Name the blood parasite species.
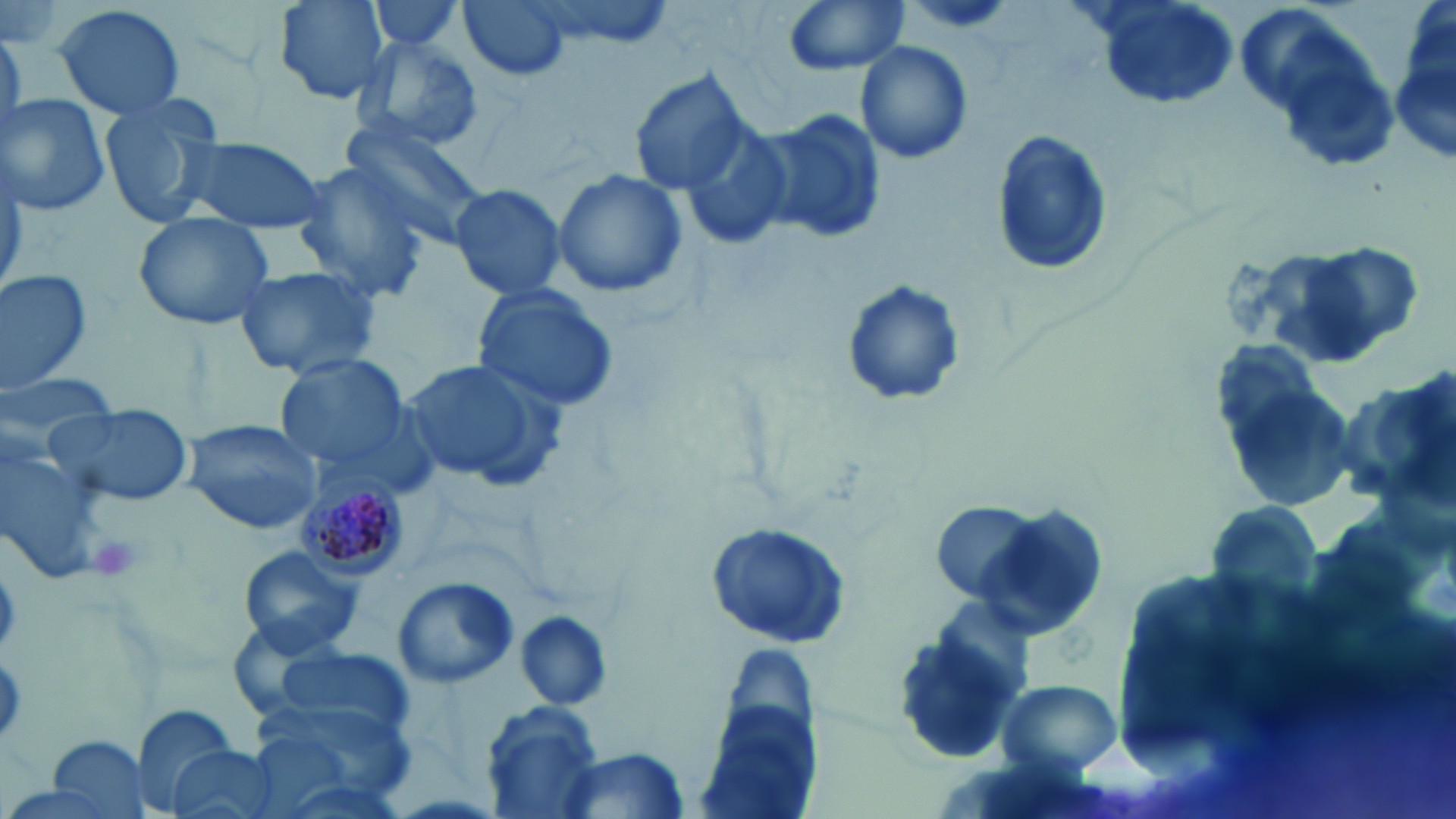

Plasmodium malariae.

Summary:
  - Coordinate format: approximate bounding boxes as [x1, y1, x2, y2] in pixels
  - Plasmodium malariae-infected red blood cell locations: [298, 480, 411, 578]
  - Platelet locations: [86, 533, 146, 584]
  - Uninfected red blood cell locations: [270, 0, 392, 104], [459, 0, 574, 84], [523, 0, 675, 54], [781, 0, 909, 75], [1232, 0, 1371, 124], [365, 1, 470, 55], [905, 3, 1015, 34], [52, 4, 189, 121], [1388, 13, 1456, 163], [350, 35, 483, 152], [854, 40, 974, 166], [1279, 47, 1402, 171], [628, 68, 753, 194], [1, 95, 112, 216], [96, 98, 226, 232], [755, 106, 887, 249], [677, 116, 799, 253], [338, 117, 491, 250], [990, 129, 1113, 276], [174, 135, 329, 234], [290, 162, 434, 303], [550, 168, 690, 299], [448, 181, 570, 302], [132, 212, 276, 332], [1286, 241, 1421, 361], [231, 265, 385, 381], [0, 267, 95, 392], [840, 280, 965, 409], [472, 285, 621, 414], [275, 353, 410, 470], [398, 356, 565, 492], [1218, 358, 1360, 518], [1348, 372, 1456, 511], [45, 403, 192, 507], [181, 418, 321, 535], [0, 437, 109, 585], [929, 501, 1051, 608], [967, 503, 1108, 644], [702, 522, 854, 650], [236, 546, 365, 657], [393, 576, 517, 691], [512, 610, 612, 710], [892, 624, 1026, 768], [270, 642, 414, 737], [998, 678, 1121, 774], [250, 701, 415, 815], [479, 701, 607, 819], [132, 704, 245, 812], [693, 705, 818, 819], [44, 736, 151, 819], [161, 743, 285, 819], [555, 748, 692, 817]
  - Field of view: one of a larger specimen
  - Image size: 1456×819 pixels
  - Magnification: 1000x
  - Stain: May-Grünwald-Giemsa
  - Modality: optical microscopy
  - Preparation: thin blood smear